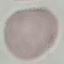
malaria status = uninfected
stain = Giemsa
capture = smartphone through the microscope eyepiece
image type = automatically extracted cell patch, resized to 64 × 64 pixels
preparation = thin smear